State which cell type is depicted.
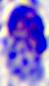

A leukocyte.

Micrograph. 400x magnification.